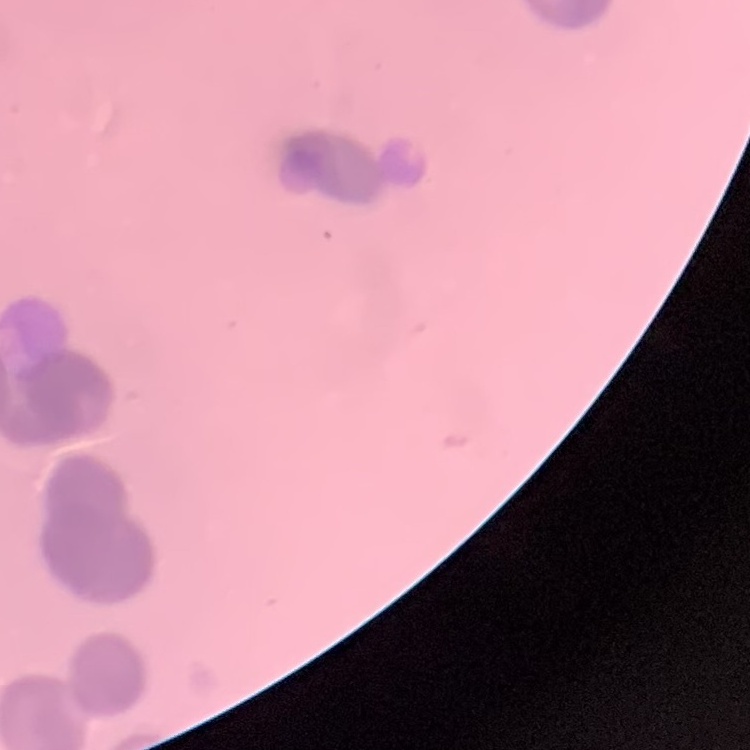
erythrocyte_morphology: rouleaux formation
image_type: square crop of a larger photomicrograph
stain: Field's or Giemsa
preparation: thin blood film